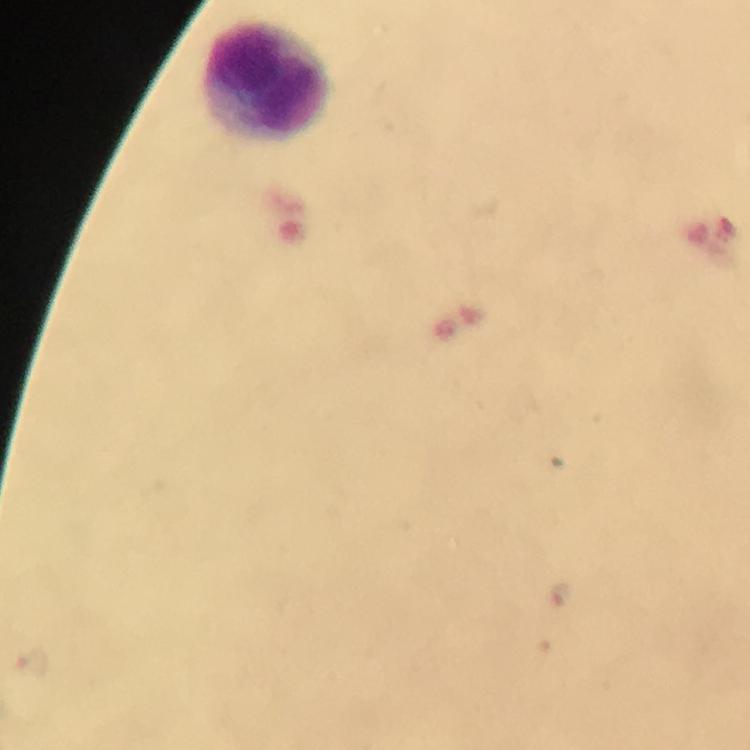 Approximate object centers, in pixels from the top-left corner. Leukocyte locations: (x=267, y=81). Image is 750×750 pixels. From a malaria diagnostic workup. Immersion oil was used. Cropped region of a single field of view. Thick blood film. Giemsa-stained preparation. Plasmodium parasites: none detected. 100x magnification. Photographed with a smartphone mounted on the microscope.